Outline each Plasmodium falciparum-infected red blood cell.
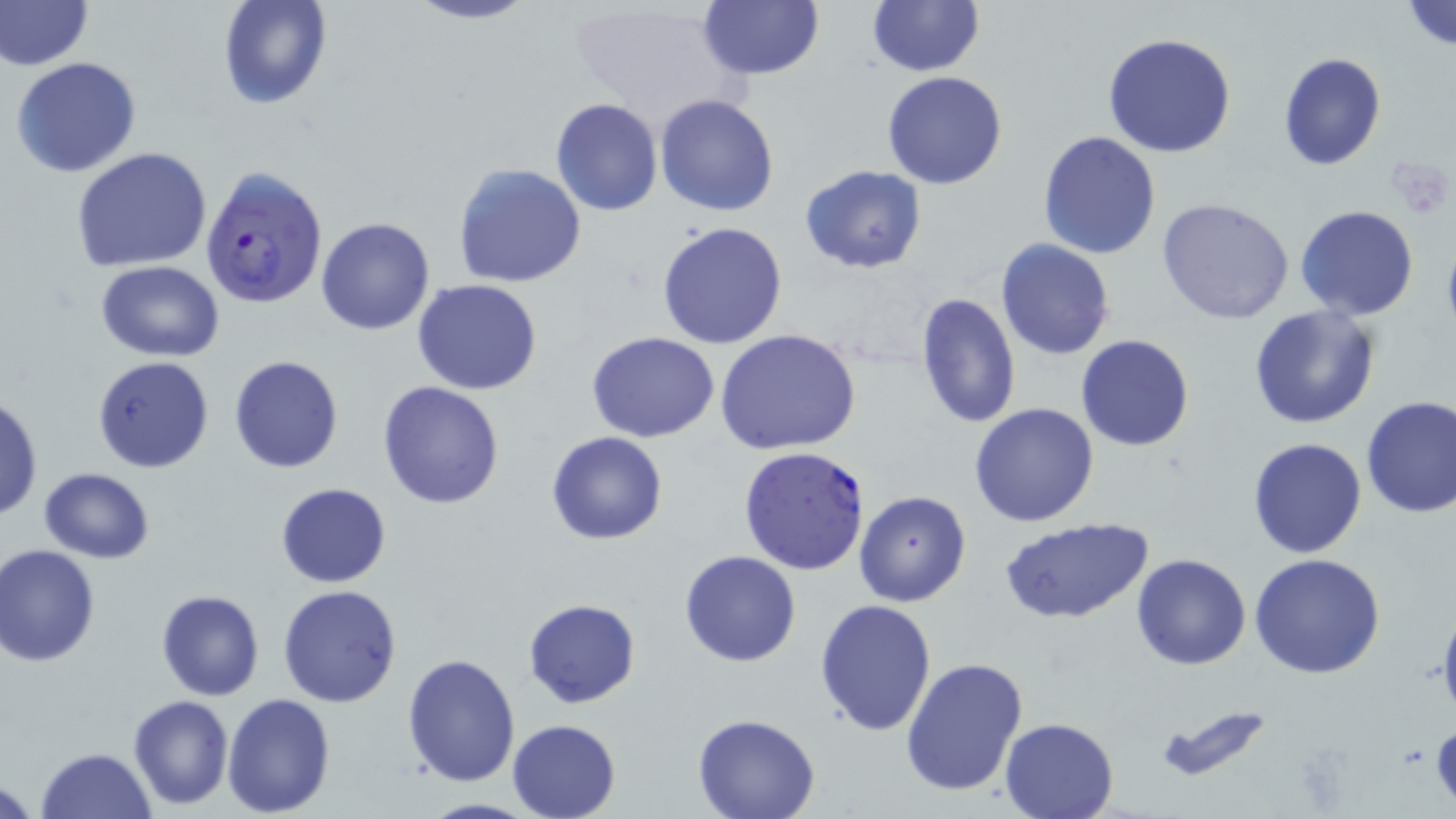

Approximate bounding boxes as (x1, y1, x2, y2) in pixels.
Plasmodium falciparum-infected red blood cells: (200, 165, 329, 308), (738, 445, 873, 578).

Uninfected red blood cell locations: (1, 0, 92, 72), (402, 0, 539, 25), (564, 0, 737, 124), (696, 0, 823, 81), (217, 1, 332, 109), (866, 1, 985, 76), (1402, 1, 1456, 54), (1102, 32, 1238, 158), (1278, 51, 1387, 170), (9, 55, 142, 178), (881, 72, 1008, 190), (655, 94, 780, 217), (550, 97, 663, 218), (1039, 131, 1162, 260), (70, 147, 213, 272), (453, 163, 586, 287), (800, 164, 926, 275), (1156, 197, 1294, 324), (1295, 205, 1419, 319), (315, 217, 435, 335), (656, 222, 789, 350), (995, 237, 1115, 361), (96, 261, 223, 361), (412, 279, 543, 396), (914, 292, 1023, 432), (1247, 304, 1383, 429), (714, 328, 861, 453), (586, 331, 721, 443), (1076, 335, 1195, 453), (229, 355, 344, 474), (91, 356, 214, 473), (377, 380, 505, 508), (1360, 395, 1455, 518), (0, 396, 43, 521), (969, 403, 1100, 526), (547, 431, 667, 545), (1246, 437, 1368, 558), (38, 468, 153, 563), (275, 483, 390, 588), (854, 490, 971, 607), (998, 517, 1156, 622), (0, 544, 101, 667), (679, 550, 801, 666), (1248, 553, 1387, 679), (1132, 554, 1252, 670), (277, 584, 402, 707), (157, 588, 264, 702), (522, 598, 640, 710), (813, 599, 937, 737), (403, 653, 522, 789), (900, 656, 1029, 799), (221, 692, 335, 817), (128, 695, 232, 810), (1154, 703, 1272, 784), (690, 714, 821, 819), (999, 717, 1120, 818), (506, 718, 623, 819), (34, 747, 158, 819). Platelet locations: (1387, 157, 1453, 220). Slide-level diagnosis: Plasmodium falciparum. May-Grünwald-Giemsa-stained preparation. Thin blood smear. One field of a larger specimen. Light microscopy. Captured at 1000x magnification. Image is 1456×819 pixels.